Report the malaria status of this cell.
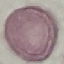

It is uninfected.

Thin blood film. Giemsa-stained preparation. Cell patch, automatically extracted from a larger field of view and resized to 64 × 64 pixels. Acquired by smartphone through the microscope eyepiece.